Assess this cell for malaria.
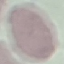

It is uninfected.

Summary:
  - Image type: cell patch, automatically extracted from a larger field of view and resized to 64 × 64 pixels
  - Preparation: thin blood smear
  - Capture: smartphone camera at the microscope eyepiece
  - Stain: Giemsa